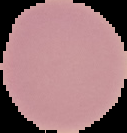

Result: negative for malaria parasites. From a thin blood film. Image is 127×133 pixels. Segmented cell region on a black background.